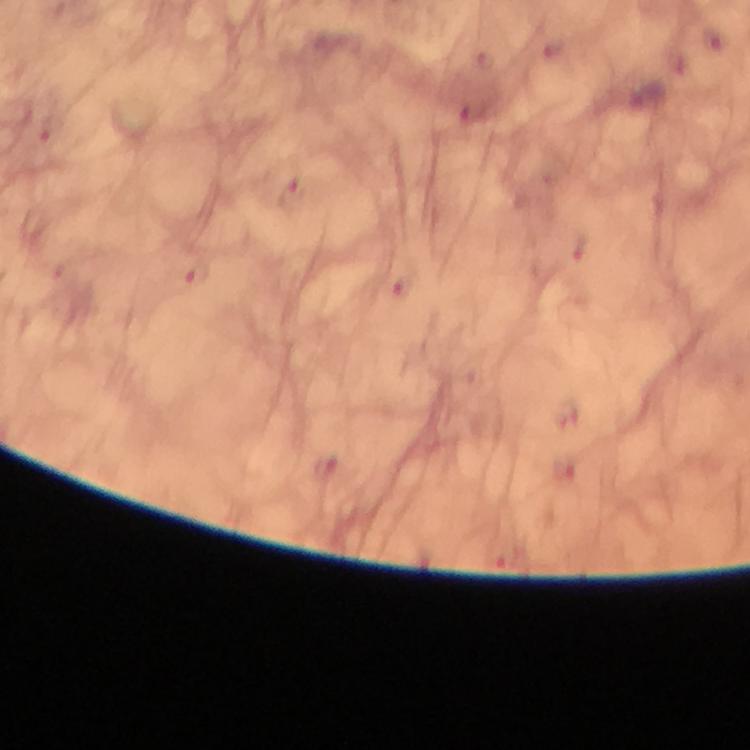

Approximate centers as {x, y} in pixels.
Summary:
  - Malaria parasite locations: {290, 195}, {196, 274}
  - Context: from a diagnostic examination for malaria
  - Immersion oil: used
  - Image size: 750×750 pixels
  - Preparation: thick blood film
  - Cropped from: one field of view
  - Stain: Giemsa
  - Magnification: 100x
  - Capture: smartphone photograph through a microscope